Locate every blood parasite and identify its species.
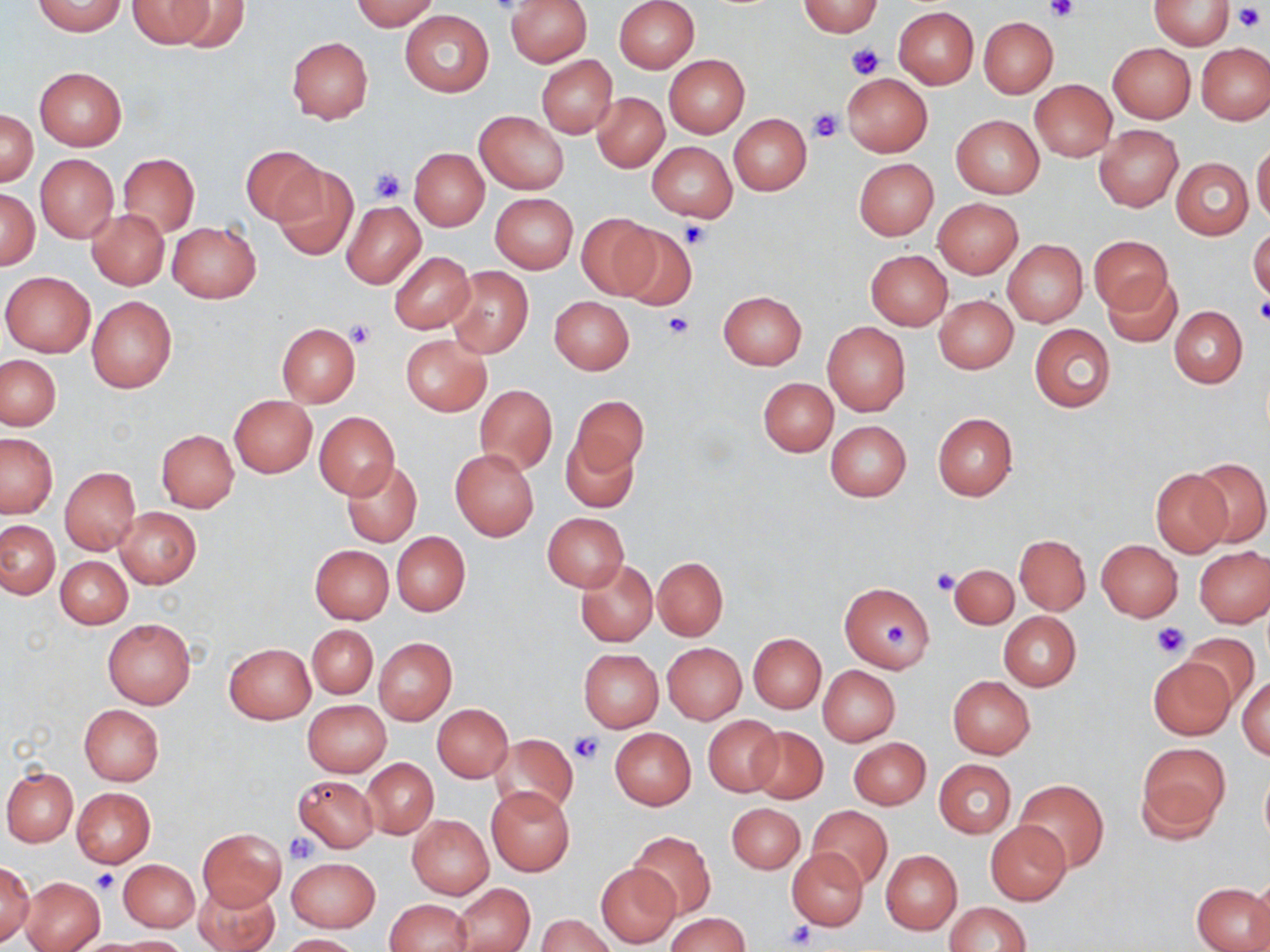
No blood parasites seen.

Approximate bounding boxes as named x1/y1/x2/y2 corners in pixels. Uninfected red blood cell locations: (x1=33, y1=0, x2=126, y2=36), (x1=127, y1=0, x2=217, y2=48), (x1=172, y1=0, x2=250, y2=52), (x1=351, y1=0, x2=438, y2=30), (x1=504, y1=0, x2=592, y2=66), (x1=614, y1=0, x2=699, y2=72), (x1=1149, y1=0, x2=1235, y2=49), (x1=798, y1=1, x2=884, y2=36), (x1=893, y1=6, x2=979, y2=88), (x1=400, y1=10, x2=494, y2=97), (x1=979, y1=17, x2=1058, y2=97), (x1=287, y1=36, x2=374, y2=123), (x1=1108, y1=43, x2=1196, y2=123), (x1=1196, y1=43, x2=1269, y2=125), (x1=536, y1=54, x2=617, y2=137), (x1=664, y1=54, x2=749, y2=138), (x1=35, y1=66, x2=126, y2=150), (x1=841, y1=73, x2=932, y2=157), (x1=1030, y1=80, x2=1117, y2=161), (x1=592, y1=92, x2=669, y2=172), (x1=1, y1=111, x2=38, y2=185), (x1=474, y1=111, x2=568, y2=194), (x1=729, y1=115, x2=810, y2=195), (x1=951, y1=115, x2=1044, y2=198), (x1=1094, y1=125, x2=1183, y2=212), (x1=647, y1=141, x2=737, y2=221), (x1=1252, y1=142, x2=1270, y2=225), (x1=241, y1=145, x2=325, y2=227), (x1=410, y1=149, x2=488, y2=230), (x1=118, y1=153, x2=199, y2=236), (x1=35, y1=154, x2=118, y2=243), (x1=853, y1=158, x2=939, y2=240), (x1=1171, y1=158, x2=1253, y2=239), (x1=271, y1=164, x2=358, y2=261), (x1=1, y1=189, x2=38, y2=268), (x1=490, y1=193, x2=577, y2=273), (x1=934, y1=198, x2=1023, y2=278), (x1=340, y1=201, x2=426, y2=288), (x1=86, y1=209, x2=170, y2=290), (x1=575, y1=214, x2=657, y2=300), (x1=167, y1=221, x2=261, y2=303), (x1=616, y1=226, x2=695, y2=313), (x1=1248, y1=227, x2=1270, y2=302), (x1=1088, y1=234, x2=1174, y2=316), (x1=1003, y1=239, x2=1088, y2=327), (x1=865, y1=250, x2=952, y2=329), (x1=389, y1=251, x2=475, y2=334), (x1=446, y1=266, x2=534, y2=358), (x1=2, y1=272, x2=95, y2=357), (x1=1103, y1=275, x2=1182, y2=347), (x1=719, y1=291, x2=806, y2=369), (x1=86, y1=296, x2=177, y2=394), (x1=550, y1=296, x2=634, y2=374), (x1=935, y1=296, x2=1018, y2=374), (x1=1171, y1=307, x2=1247, y2=387), (x1=821, y1=322, x2=910, y2=415), (x1=277, y1=324, x2=360, y2=406), (x1=1029, y1=325, x2=1114, y2=412), (x1=401, y1=334, x2=490, y2=415), (x1=1, y1=355, x2=61, y2=429), (x1=758, y1=377, x2=837, y2=456), (x1=474, y1=385, x2=557, y2=474), (x1=230, y1=395, x2=316, y2=478), (x1=570, y1=395, x2=648, y2=476), (x1=314, y1=411, x2=399, y2=500), (x1=933, y1=413, x2=1017, y2=501), (x1=826, y1=420, x2=912, y2=501), (x1=156, y1=430, x2=239, y2=512), (x1=560, y1=431, x2=640, y2=513), (x1=0, y1=432, x2=57, y2=517), (x1=450, y1=448, x2=539, y2=541), (x1=1191, y1=459, x2=1270, y2=547), (x1=339, y1=460, x2=423, y2=548), (x1=61, y1=466, x2=140, y2=554), (x1=1150, y1=468, x2=1232, y2=557), (x1=116, y1=507, x2=201, y2=589), (x1=543, y1=513, x2=629, y2=591), (x1=0, y1=521, x2=59, y2=598), (x1=392, y1=532, x2=470, y2=615), (x1=1015, y1=534, x2=1090, y2=614), (x1=1096, y1=540, x2=1183, y2=622), (x1=310, y1=544, x2=394, y2=624), (x1=1195, y1=547, x2=1270, y2=628), (x1=54, y1=555, x2=131, y2=629), (x1=651, y1=556, x2=729, y2=640), (x1=575, y1=560, x2=657, y2=646), (x1=949, y1=563, x2=1019, y2=629), (x1=840, y1=582, x2=935, y2=673), (x1=999, y1=611, x2=1081, y2=691), (x1=102, y1=617, x2=196, y2=708), (x1=307, y1=624, x2=378, y2=700), (x1=749, y1=632, x2=826, y2=713), (x1=1182, y1=633, x2=1259, y2=704), (x1=374, y1=638, x2=456, y2=724), (x1=225, y1=643, x2=315, y2=723), (x1=663, y1=643, x2=746, y2=724), (x1=579, y1=649, x2=663, y2=732), (x1=1149, y1=657, x2=1236, y2=739), (x1=818, y1=665, x2=900, y2=746), (x1=1237, y1=675, x2=1270, y2=759), (x1=947, y1=676, x2=1035, y2=759), (x1=302, y1=700, x2=391, y2=777), (x1=80, y1=704, x2=164, y2=785), (x1=433, y1=704, x2=513, y2=781), (x1=703, y1=716, x2=782, y2=795), (x1=749, y1=726, x2=827, y2=803), (x1=610, y1=728, x2=696, y2=810), (x1=492, y1=734, x2=579, y2=816), (x1=849, y1=738, x2=930, y2=809), (x1=1136, y1=743, x2=1230, y2=840), (x1=362, y1=758, x2=438, y2=838), (x1=934, y1=759, x2=1016, y2=837), (x1=3, y1=766, x2=78, y2=846), (x1=1260, y1=769, x2=1270, y2=848), (x1=294, y1=775, x2=378, y2=852), (x1=1015, y1=779, x2=1108, y2=872), (x1=73, y1=787, x2=156, y2=866), (x1=486, y1=787, x2=574, y2=875), (x1=727, y1=803, x2=804, y2=874), (x1=807, y1=806, x2=892, y2=888), (x1=407, y1=815, x2=493, y2=899), (x1=985, y1=820, x2=1071, y2=904), (x1=198, y1=827, x2=286, y2=911), (x1=630, y1=831, x2=715, y2=919), (x1=789, y1=848, x2=867, y2=929), (x1=881, y1=849, x2=961, y2=935), (x1=287, y1=857, x2=380, y2=932), (x1=119, y1=859, x2=200, y2=932), (x1=0, y1=862, x2=36, y2=944), (x1=596, y1=863, x2=680, y2=948), (x1=1249, y1=872, x2=1270, y2=952), (x1=20, y1=876, x2=106, y2=952), (x1=193, y1=878, x2=282, y2=952), (x1=452, y1=883, x2=534, y2=952), (x1=1192, y1=883, x2=1268, y2=952), (x1=384, y1=899, x2=473, y2=952), (x1=945, y1=902, x2=1032, y2=952), (x1=665, y1=912, x2=751, y2=952), (x1=538, y1=914, x2=615, y2=952), (x1=280, y1=933, x2=362, y2=952), (x1=110, y1=936, x2=191, y2=951). Platelet locations: (x1=1045, y1=0, x2=1078, y2=22), (x1=1233, y1=3, x2=1267, y2=33), (x1=848, y1=44, x2=883, y2=79), (x1=808, y1=107, x2=843, y2=143), (x1=371, y1=168, x2=405, y2=203), (x1=680, y1=222, x2=711, y2=250), (x1=1254, y1=299, x2=1270, y2=327), (x1=661, y1=312, x2=695, y2=339), (x1=346, y1=320, x2=376, y2=348), (x1=931, y1=568, x2=959, y2=595), (x1=1149, y1=620, x2=1191, y2=658), (x1=883, y1=624, x2=914, y2=648), (x1=569, y1=733, x2=602, y2=763), (x1=286, y1=833, x2=318, y2=862), (x1=92, y1=869, x2=120, y2=893), (x1=784, y1=920, x2=816, y2=948). Slide-level diagnosis: no evidence of blood parasites. 1000x magnification. Optical microscopy. Single field of view. Thin blood smear. May-Grünwald-Giemsa stain. Image is 1270×952 pixels.